Assess this cell for malaria.
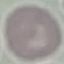

It is uninfected.

Summary:
  - Image type: automatically extracted cell patch, resized to 64 × 64 pixels
  - Capture: smartphone camera at the microscope eyepiece
  - Preparation: thin blood film
  - Stain: Giemsa